Assess for Plasmodium parasites.
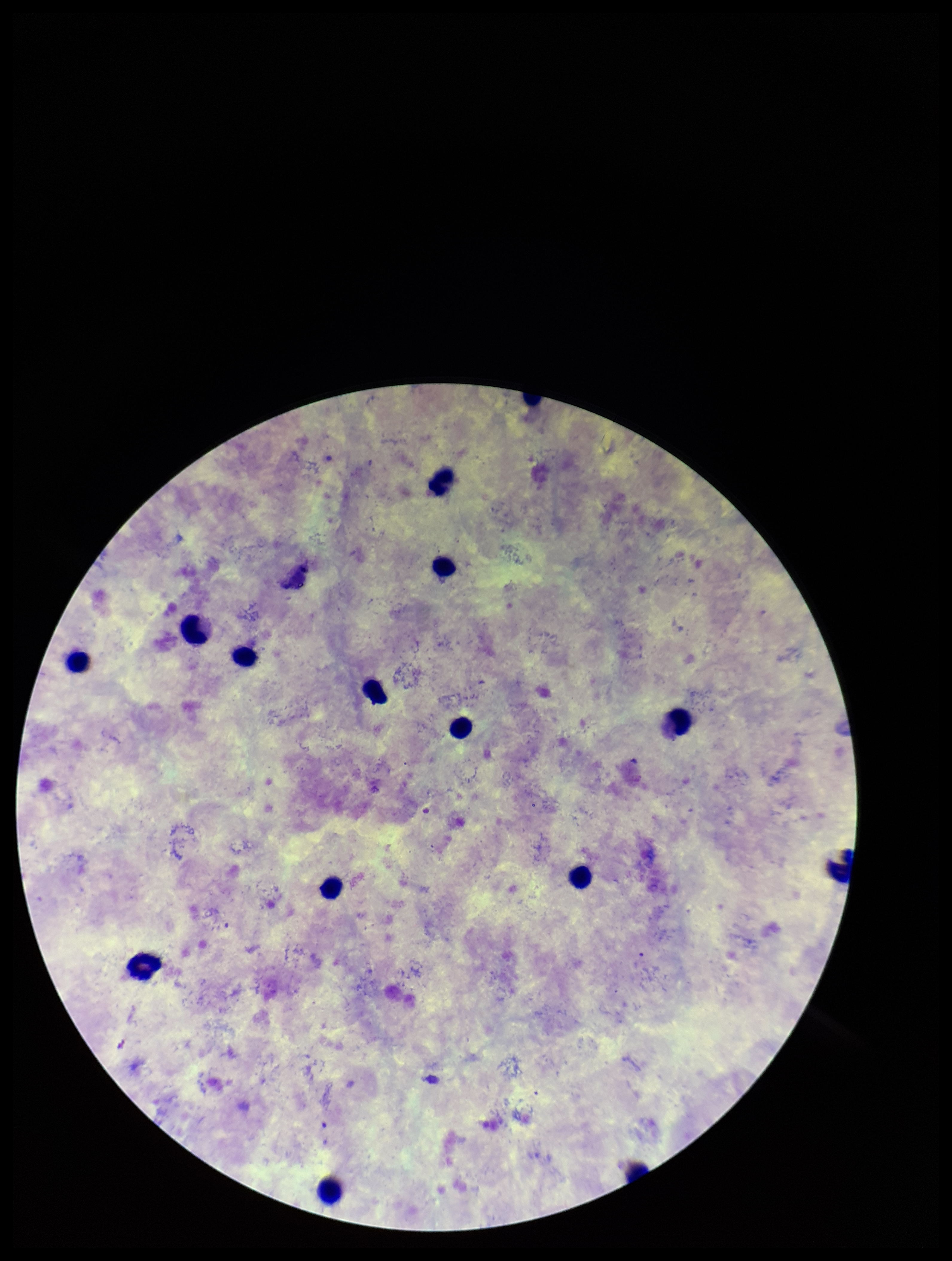

None detected.

leukocyte_count: 14
parasite_count: 0
capture: smartphone photograph through the microscope eyepiece
patient_malaria_status: positive
preparation: thick blood smear
field_of_view: one from this slide
image_size: 952×1261 pixels
stain: Giemsa
species_reported_for_this_patient: Plasmodium vivax